Give the location of every parasitized RBC.
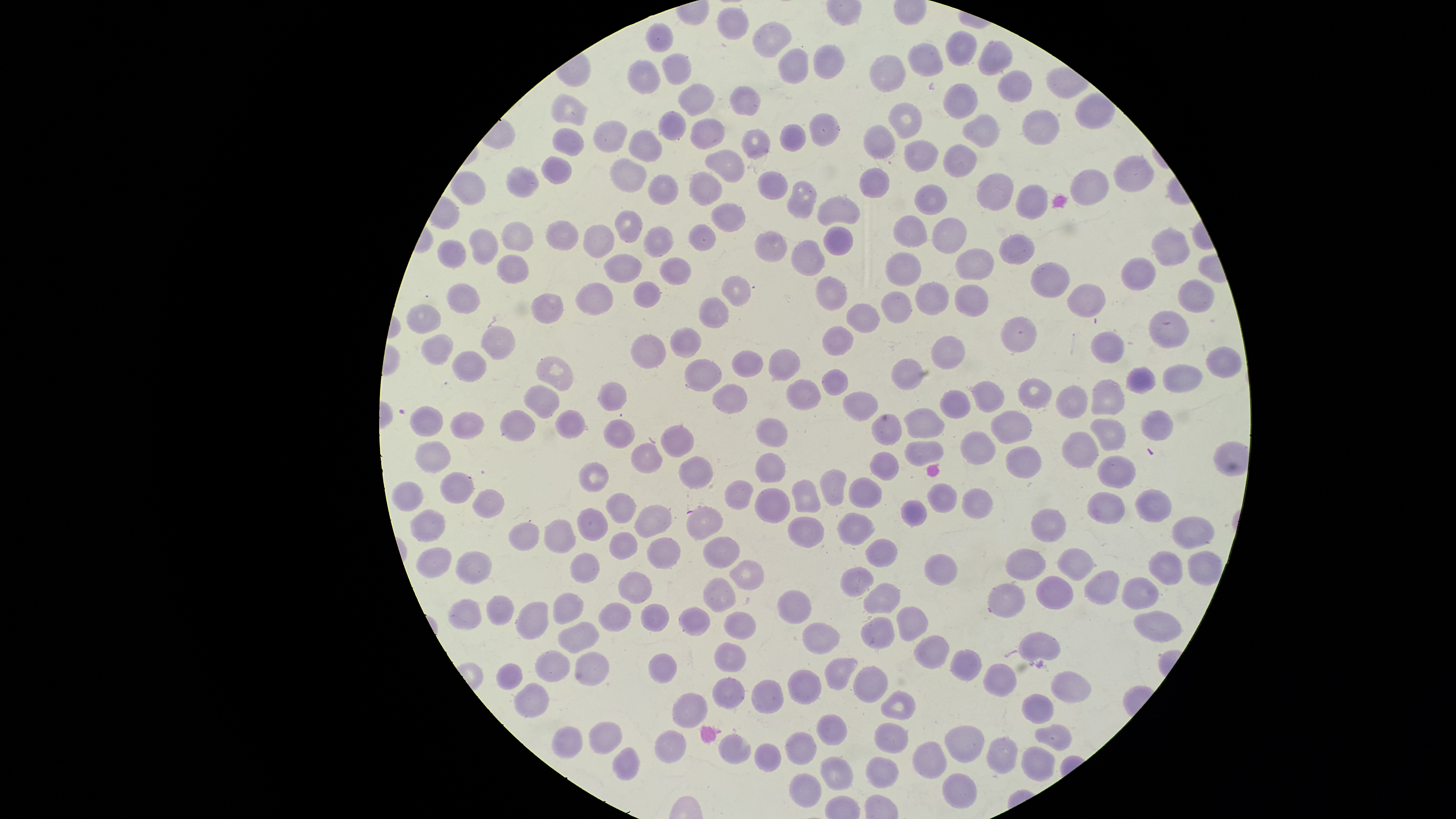
No parasitized RBCs identified.

Approximate bounding boxes as {left, top, right, bottom} in pixels.
Summary:
  - Uninfected RBCs: {715, 8, 749, 40}, {751, 22, 792, 58}, {645, 23, 673, 53}, {945, 31, 978, 67}, {979, 40, 1013, 76}, {908, 42, 945, 78}, {814, 45, 846, 79}, {777, 48, 808, 84}, {661, 53, 691, 86}, {870, 54, 907, 92}, {627, 59, 660, 95}, {997, 70, 1032, 103}, {943, 82, 978, 120}, {677, 83, 715, 118}, {730, 87, 760, 117}, {550, 94, 589, 128}, {888, 101, 922, 140}, {659, 110, 687, 141}, {1022, 110, 1060, 146}, {809, 112, 839, 147}, {963, 114, 1000, 149}, {690, 119, 725, 151}, {592, 120, 628, 153}, {779, 124, 806, 152}, {863, 124, 896, 160}, {552, 128, 585, 156}, {740, 128, 770, 160}, {628, 130, 662, 163}, {904, 139, 939, 172}, {943, 144, 978, 179}, {705, 149, 744, 182}, {541, 156, 572, 184}, {1113, 156, 1153, 193}, {611, 157, 646, 193}, {505, 166, 538, 199}, {858, 167, 891, 199}, {1069, 169, 1110, 206}, {451, 170, 485, 206}, {688, 171, 722, 206}, {756, 171, 790, 200}, {977, 173, 1014, 212}, {647, 175, 678, 204}, {786, 181, 818, 219}, {913, 183, 948, 216}, {1016, 184, 1048, 220}, {816, 197, 861, 226}, {712, 203, 746, 232}, {614, 210, 642, 243}, {892, 215, 927, 248}, {932, 216, 967, 255}, {546, 220, 579, 252}, {501, 221, 533, 252}, {582, 224, 616, 258}, {688, 224, 715, 252}, {823, 225, 852, 256}, {642, 226, 673, 258}, {1151, 227, 1190, 267}, {468, 228, 499, 264}, {754, 229, 788, 263}, {999, 233, 1035, 265}, {437, 239, 467, 268}, {791, 239, 825, 277}, {956, 246, 994, 280}, {885, 251, 922, 286}, {496, 254, 530, 283}, {603, 254, 642, 283}, {1120, 256, 1156, 292}, {659, 258, 692, 286}, {1031, 261, 1070, 298}, {721, 276, 753, 306}, {815, 277, 847, 311}, {1178, 279, 1215, 314}, {632, 281, 661, 308}, {575, 282, 614, 316}, {914, 282, 948, 315}, {446, 283, 480, 315}, {1067, 283, 1105, 318}, {954, 284, 988, 317}, {880, 291, 912, 325}, {530, 293, 564, 323}, {698, 297, 729, 329}, {406, 303, 440, 334}, {846, 303, 881, 334}, {1149, 309, 1189, 349}, {1000, 315, 1037, 354}, {822, 324, 854, 357}, {480, 326, 517, 361}, {669, 326, 702, 359}, {1091, 330, 1124, 364}, {420, 334, 454, 365}, {632, 334, 666, 371}, {931, 335, 965, 369}, {1206, 346, 1241, 379}, {768, 349, 800, 381}, {731, 350, 764, 378}, {536, 356, 573, 392}, {891, 357, 923, 390}, {685, 358, 721, 392}, {1162, 363, 1202, 393}, {1127, 367, 1155, 394}, {822, 368, 847, 397}, {1018, 377, 1052, 409}, {785, 379, 822, 411}, {972, 379, 1005, 413}, {1089, 379, 1124, 419}, {596, 382, 626, 412}, {524, 384, 560, 419}, {714, 384, 748, 414}, {1055, 385, 1088, 418}, {940, 389, 970, 418}, {843, 391, 878, 421}, {409, 405, 444, 437}, {903, 407, 945, 439}, {1140, 409, 1173, 440}, {499, 410, 536, 441}, {554, 410, 585, 439}, {991, 410, 1031, 444}, {450, 411, 485, 439}, {871, 414, 901, 446}, {755, 418, 787, 449}, {1088, 419, 1126, 451}, {604, 420, 635, 449}, {660, 425, 694, 456}, {960, 431, 995, 465}, {1062, 431, 1099, 469}, {414, 441, 452, 472}, {903, 441, 943, 467}, {632, 443, 663, 474}, {1006, 445, 1041, 479}, {869, 450, 899, 481}, {755, 454, 787, 484}, {1097, 455, 1135, 488}, {679, 456, 714, 489}, {577, 461, 609, 492}, {819, 469, 847, 506}, {439, 472, 474, 505}, {848, 477, 882, 509}, {791, 478, 821, 515}, {724, 480, 752, 509}, {391, 482, 423, 511}, {927, 483, 957, 514}, {753, 487, 790, 523}, {961, 487, 991, 519}, {472, 489, 505, 518}, {1134, 489, 1171, 523}, {1087, 491, 1125, 525}, {605, 493, 636, 524}, {900, 500, 926, 527}, {634, 504, 673, 538}, {686, 506, 724, 540}, {577, 507, 608, 542}, {410, 509, 446, 542}, {1031, 509, 1066, 543}, {837, 512, 875, 546}, {787, 517, 824, 548}, {1171, 517, 1214, 549}, {544, 519, 575, 553}, {508, 521, 540, 551}, {608, 532, 636, 560}, {647, 537, 681, 569}, {702, 537, 740, 569}, {865, 539, 899, 568}, {415, 547, 452, 578}, {1057, 548, 1095, 581}, {1004, 549, 1046, 581}, {454, 550, 493, 584}, {1187, 550, 1223, 585}, {1148, 551, 1184, 585}, {569, 552, 600, 583}, {924, 554, 960, 586}, {729, 559, 764, 591}, {840, 566, 874, 596}, {617, 571, 653, 604}, {1085, 571, 1121, 605}, {1036, 576, 1075, 609}, {703, 577, 736, 612}, {1122, 577, 1159, 610}, {864, 582, 900, 616}, {987, 582, 1024, 618}, {779, 589, 811, 624}, {553, 593, 584, 624}, {486, 596, 514, 627}, {447, 597, 481, 631}, {515, 600, 550, 641}, {598, 601, 632, 633}, {640, 604, 669, 631}, {679, 605, 711, 635}, {895, 605, 928, 640}, {723, 611, 756, 640}, {1132, 611, 1183, 641}, {861, 616, 893, 650}, {558, 621, 599, 654}, {803, 623, 841, 655}, {1016, 631, 1060, 663}, {914, 635, 950, 669}, {714, 642, 747, 673}, {534, 649, 570, 683}, {950, 649, 981, 681}, {575, 651, 609, 687}, {648, 653, 677, 684}, {824, 657, 859, 689}, {496, 662, 522, 692}, {983, 664, 1017, 698}, {852, 666, 888, 703}, {787, 669, 822, 706}, {1051, 671, 1092, 703}, {712, 677, 745, 709}, {752, 679, 783, 715}, {514, 683, 549, 718}, {882, 690, 916, 720}, {1021, 692, 1054, 724}, {673, 693, 706, 729}, {817, 714, 848, 746}, {590, 721, 624, 754}, {873, 722, 909, 754}, {1033, 724, 1072, 751}, {944, 725, 983, 763}, {551, 726, 583, 759}, {655, 729, 686, 764}, {786, 732, 816, 767}, {718, 734, 752, 764}, {986, 737, 1017, 774}, {754, 742, 782, 772}, {912, 742, 947, 778}, {1022, 745, 1054, 781}, {612, 747, 641, 780}, {820, 755, 854, 791}, {866, 758, 899, 789}, {789, 772, 822, 808}, {943, 773, 977, 809}
  - Stain: Giemsa
  - Field of view: single
  - Visible region: circular
  - Image size: 1456×819 pixels
  - Capture: smartphone photograph through the microscope eyepiece
  - Preparation: thin blood film